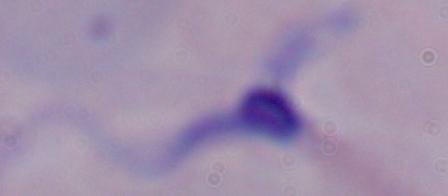
A trypanosome is seen. Micrograph. 1000x magnification.